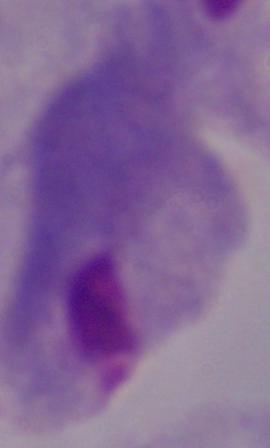

Summary:
  - Magnification: 1000x
  - Modality: micrograph
  - Identification: trichomonad